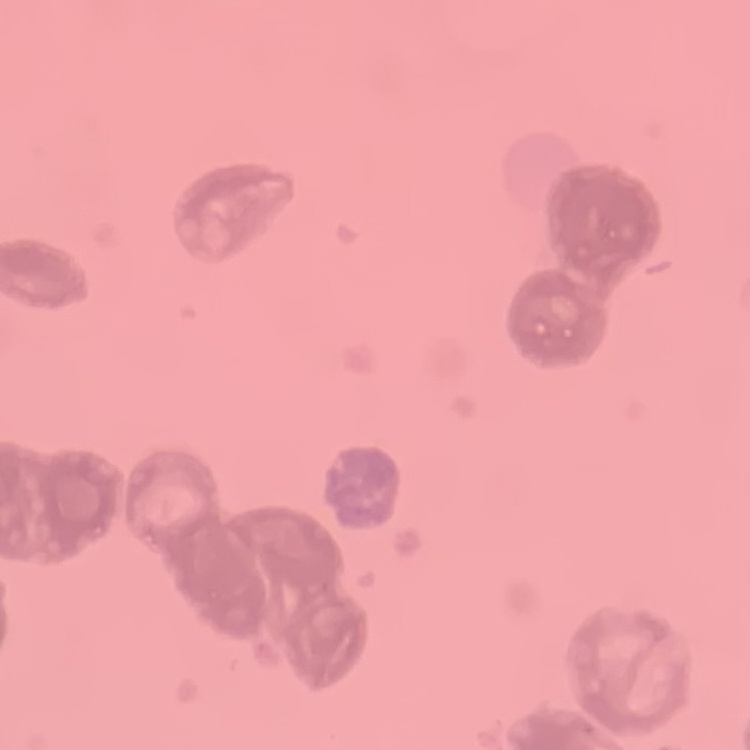
red_blood_cell_morphology: rouleaux formation
preparation: thin blood film
image_type: one tile cut from a larger photomicrograph
stain: Field's or Giemsa